Report the malaria status of this cell.
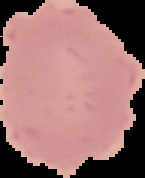
Uninfected.

Summary:
  - Preparation: thin blood film
  - Image size: 145×178 pixels
  - Image type: segmented cell region on a black background